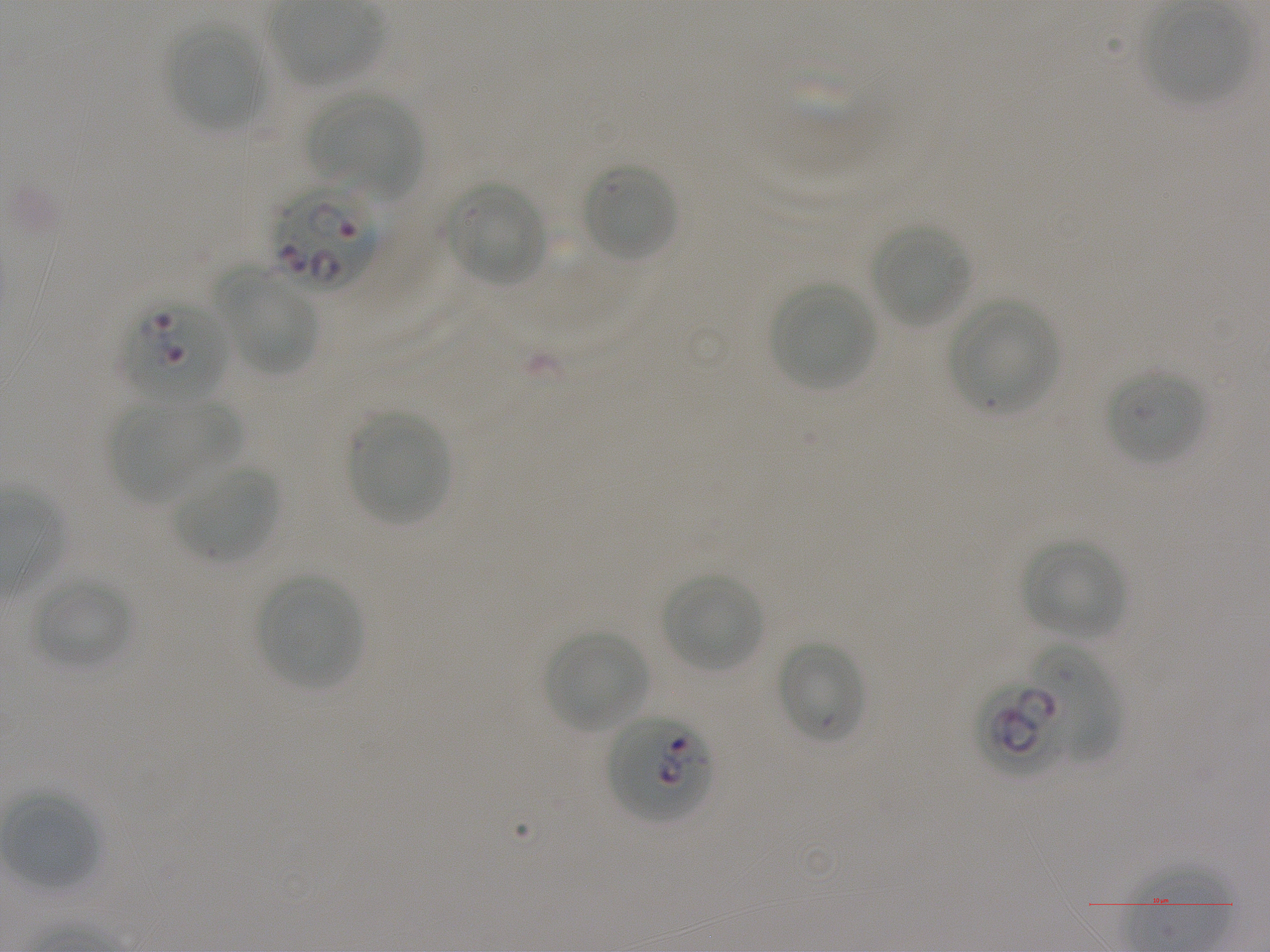

Approximate bounding rectangles given as corner coordinates in pixels from the top-left. Not every red blood cell is marked.
Summary:
  - Locations of uninfected red blood cells: (x1=1144, y1=6, x2=1252, y2=105), (x1=167, y1=25, x2=265, y2=129), (x1=313, y1=90, x2=420, y2=196), (x1=582, y1=162, x2=678, y2=263), (x1=446, y1=181, x2=549, y2=287), (x1=870, y1=223, x2=972, y2=326), (x1=230, y1=277, x2=318, y2=377), (x1=771, y1=283, x2=875, y2=389), (x1=949, y1=298, x2=1060, y2=412), (x1=1107, y1=368, x2=1206, y2=466), (x1=182, y1=402, x2=246, y2=468), (x1=109, y1=404, x2=198, y2=505), (x1=347, y1=411, x2=451, y2=525), (x1=175, y1=463, x2=279, y2=562), (x1=1023, y1=538, x2=1126, y2=638), (x1=662, y1=572, x2=764, y2=673), (x1=256, y1=574, x2=363, y2=689), (x1=30, y1=575, x2=133, y2=669), (x1=545, y1=630, x2=649, y2=732), (x1=776, y1=639, x2=865, y2=743), (x1=2, y1=792, x2=100, y2=890)
  - Locations of red blood cells of indeterminate infection status: (x1=1026, y1=642, x2=1120, y2=764)
  - Locations of infected red blood cells: (x1=269, y1=183, x2=381, y2=288), (x1=124, y1=299, x2=228, y2=404), (x1=972, y1=681, x2=1076, y2=774), (x1=606, y1=714, x2=714, y2=824)
  - Donor blood group: A+
  - Stain: Giemsa
  - Image size: 1270×952 pixels
  - Culture: static in-vitro P. falciparum strain NF54
  - Field of view: one from this slide
  - Preparation: thin blood film
  - Objective: 100x, oil immersion, numerical aperture 1.25